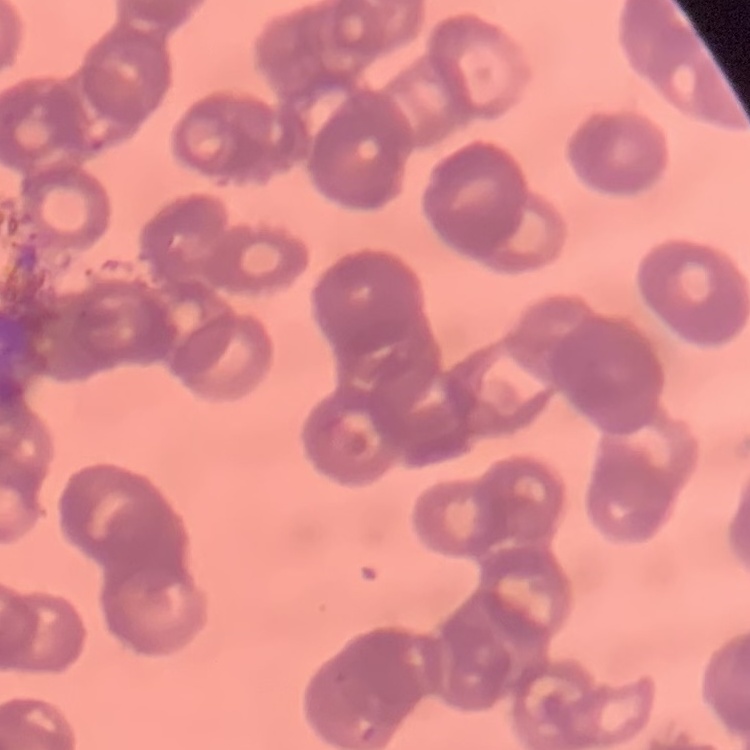

Summary:
  - Red blood cell morphology: rouleaux formation
  - Stain: Field's or Giemsa
  - Preparation: thin blood film
  - Image type: one tile cut from a larger photomicrograph